Report the malaria status of this cell.
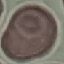
Uninfected.

Thin smear of blood. Giemsa-stained preparation. Cell patch, automatically extracted from a larger field of view and resized to 64 × 64 pixels. Photographed with a smartphone camera at the microscope eyepiece.